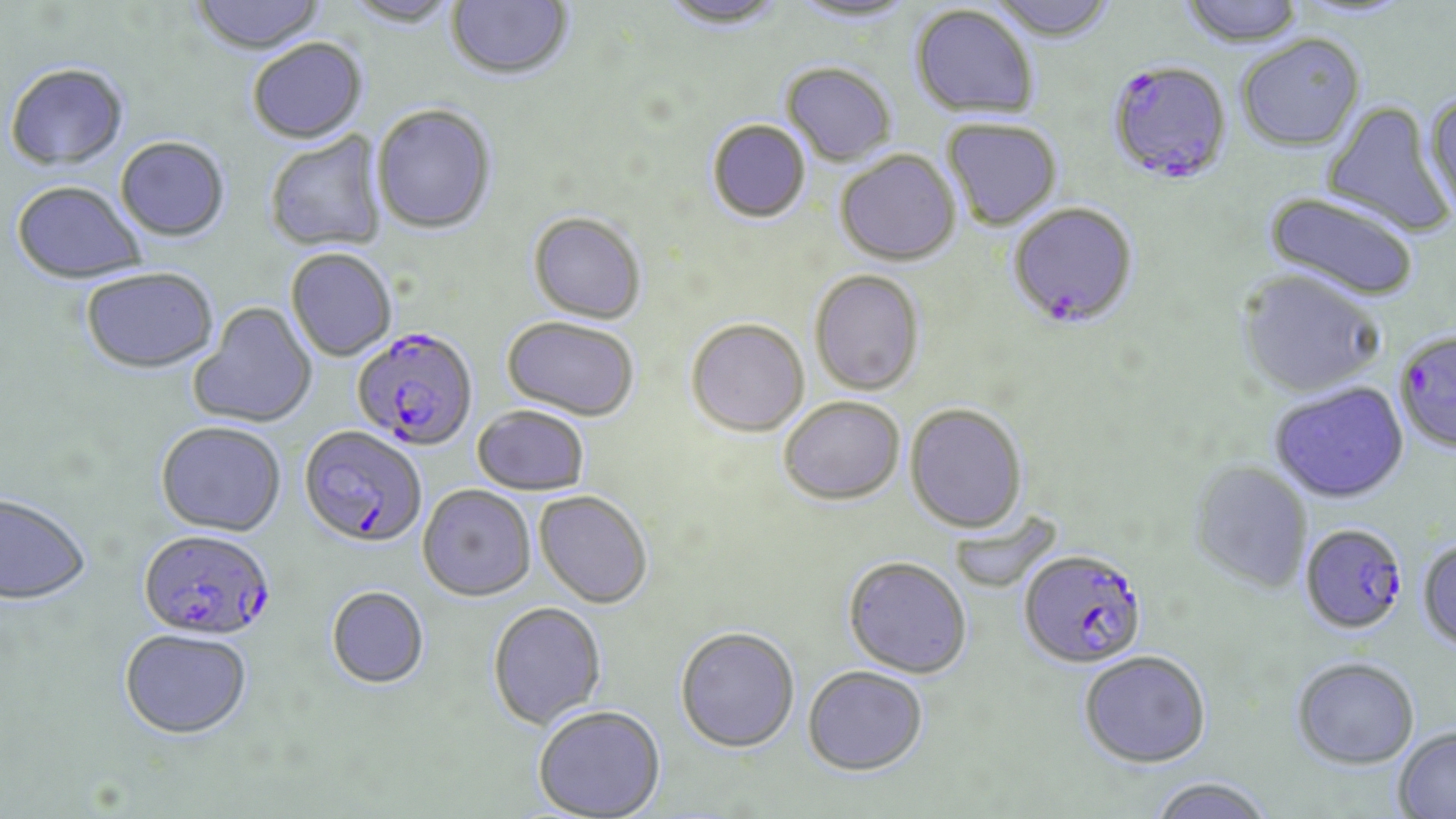

Approximate bounding boxes as named x1/y1/x2/y2 corners in pixels. Uninfected red blood cell locations: (x1=189, y1=0, x2=328, y2=57), (x1=343, y1=0, x2=460, y2=29), (x1=446, y1=0, x2=574, y2=83), (x1=658, y1=0, x2=790, y2=31), (x1=788, y1=0, x2=920, y2=25), (x1=987, y1=0, x2=1119, y2=42), (x1=1176, y1=0, x2=1307, y2=48), (x1=910, y1=4, x2=1040, y2=118), (x1=1236, y1=34, x2=1366, y2=152), (x1=248, y1=40, x2=368, y2=146), (x1=780, y1=63, x2=896, y2=168), (x1=4, y1=65, x2=130, y2=175), (x1=1422, y1=92, x2=1456, y2=221), (x1=1321, y1=100, x2=1454, y2=239), (x1=371, y1=106, x2=498, y2=237), (x1=941, y1=118, x2=1062, y2=230), (x1=707, y1=120, x2=810, y2=224), (x1=265, y1=134, x2=387, y2=254), (x1=115, y1=138, x2=230, y2=244), (x1=835, y1=150, x2=961, y2=267), (x1=11, y1=184, x2=147, y2=287), (x1=1262, y1=192, x2=1420, y2=302), (x1=528, y1=213, x2=646, y2=325), (x1=285, y1=250, x2=396, y2=362), (x1=809, y1=269, x2=924, y2=396), (x1=1236, y1=269, x2=1385, y2=399), (x1=80, y1=270, x2=219, y2=377), (x1=188, y1=303, x2=318, y2=429), (x1=501, y1=317, x2=639, y2=422), (x1=686, y1=320, x2=809, y2=438), (x1=1269, y1=383, x2=1408, y2=503), (x1=778, y1=396, x2=906, y2=505), (x1=904, y1=404, x2=1028, y2=534), (x1=473, y1=407, x2=589, y2=497), (x1=156, y1=423, x2=286, y2=538), (x1=1188, y1=460, x2=1313, y2=594), (x1=418, y1=486, x2=536, y2=602), (x1=534, y1=491, x2=652, y2=609), (x1=0, y1=494, x2=92, y2=607), (x1=948, y1=509, x2=1060, y2=594), (x1=1417, y1=538, x2=1456, y2=653), (x1=843, y1=556, x2=972, y2=678), (x1=326, y1=587, x2=429, y2=689), (x1=487, y1=602, x2=607, y2=729), (x1=675, y1=627, x2=800, y2=754), (x1=118, y1=628, x2=253, y2=739), (x1=1079, y1=650, x2=1211, y2=767), (x1=1291, y1=657, x2=1420, y2=769), (x1=803, y1=666, x2=929, y2=775), (x1=532, y1=707, x2=666, y2=819), (x1=1393, y1=727, x2=1456, y2=818), (x1=1146, y1=776, x2=1274, y2=819). Plasmodium falciparum-infected red blood cell locations: (x1=1107, y1=59, x2=1233, y2=184), (x1=1007, y1=202, x2=1139, y2=328), (x1=350, y1=328, x2=477, y2=453), (x1=1394, y1=329, x2=1456, y2=455), (x1=297, y1=427, x2=426, y2=549), (x1=1300, y1=524, x2=1407, y2=634), (x1=137, y1=529, x2=275, y2=642), (x1=1019, y1=548, x2=1148, y2=669). Slide-level diagnosis: Plasmodium falciparum. Image is 1456×819 pixels. Thin blood smear. May-Grünwald-Giemsa-stained preparation. Light microscopy. Single field of view. Captured at 1000x magnification.